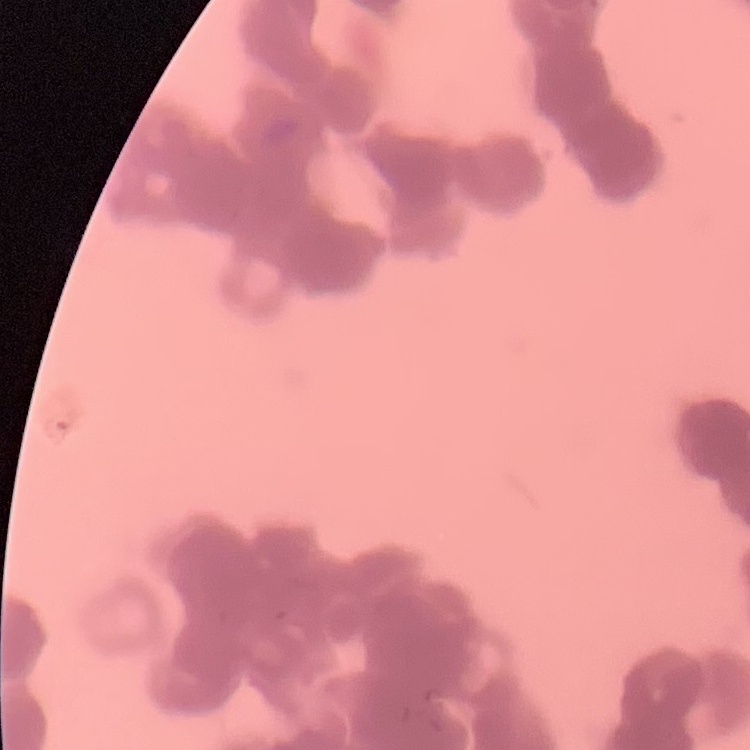 The erythrocytes exhibit rouleaux formation. Field's or Giemsa stain. One tile cut from a larger photomicrograph. Thin blood smear.